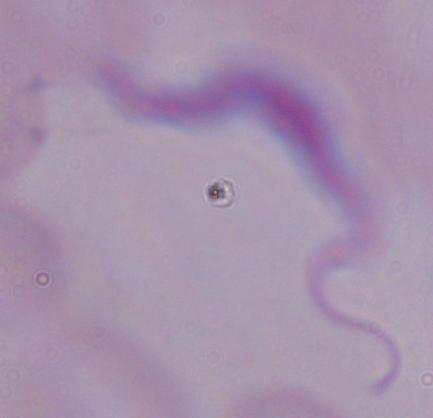

Summary:
  - Modality: micrograph
  - Magnification: 1000x
  - Identification: trypanosome